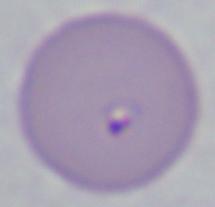

identification = Babesia
magnification = 1000x
modality = photomicrograph